Identify the cell.
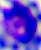

A leukocyte.

modality = micrograph
magnification = 400x